Point out each Plasmodium parasite.
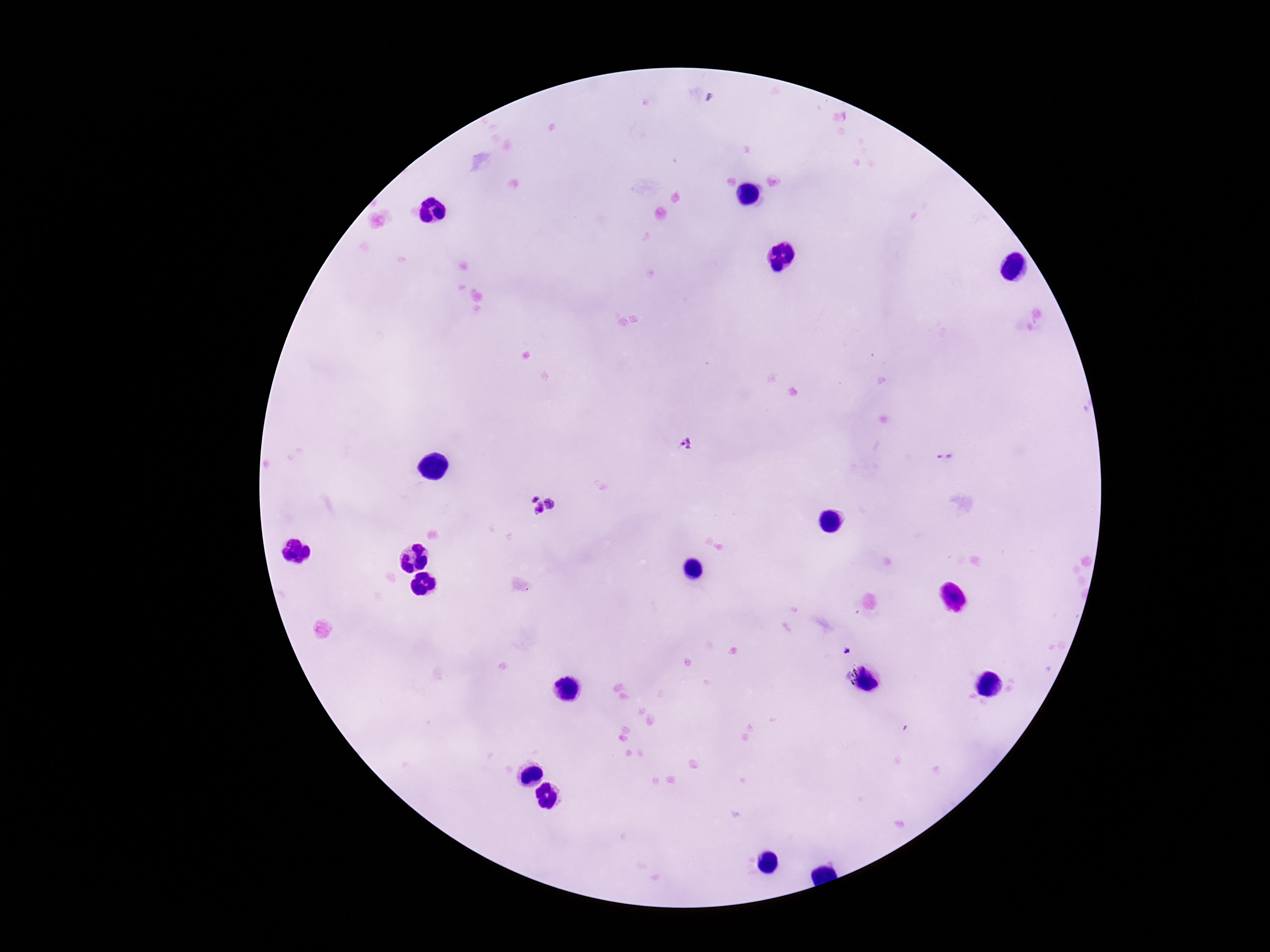

Approximate object centers, in pixels from the top-left corner.
Plasmodium parasites: (x=686, y=443), (x=848, y=651).

Photographed through the microscope eyepiece with a smartphone camera. Giemsa-stained preparation. Patient malaria status: infected. Image is 1270×952 pixels. 100x magnification. Thick blood film. Single field of view.